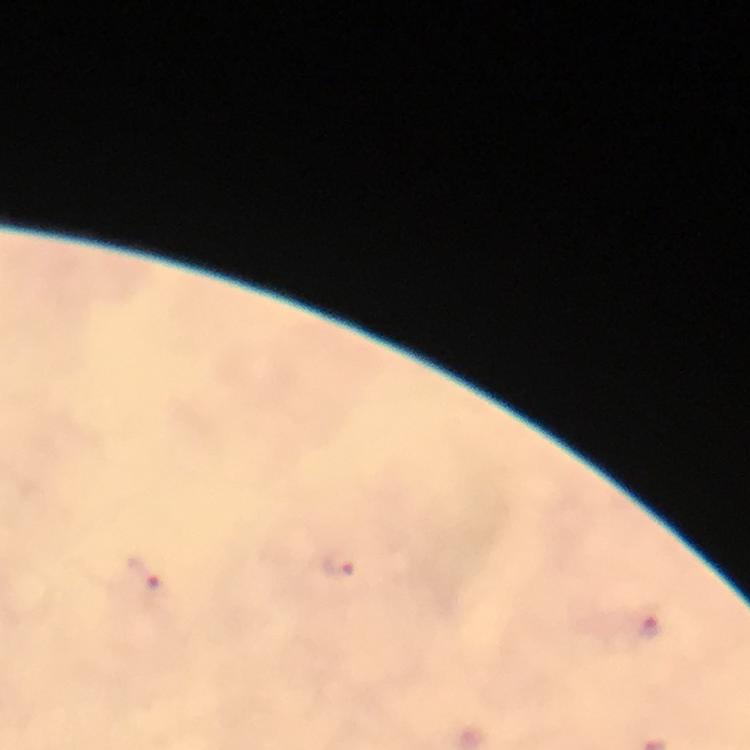
Approximate centers as {x, y} in pixels.
Summary:
  - Malaria parasite locations: {339, 566}, {144, 572}, {653, 627}
  - Context: from a diagnostic examination for malaria
  - Stain: Giemsa
  - Capture: smartphone photograph through a microscope
  - Cropped from: one field of view
  - Immersion oil: applied
  - Image size: 750×750 pixels
  - Magnification: 100x
  - Preparation: thick smear